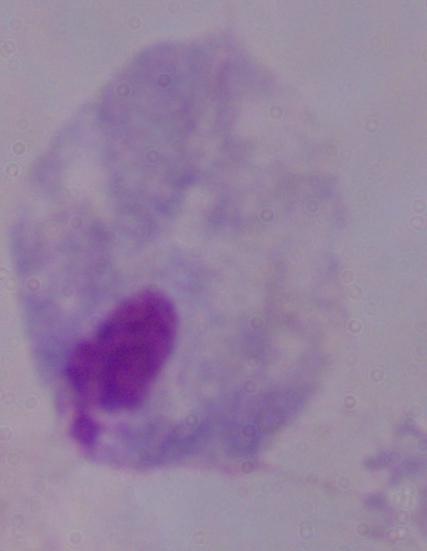 1000x magnification. A trichomonad is seen. Photomicrograph.